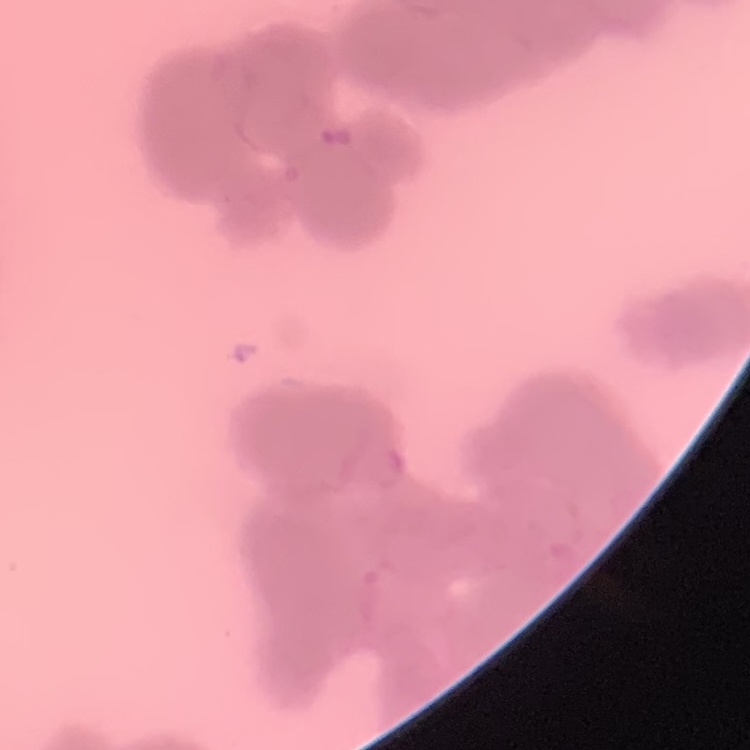

The erythrocytes show rouleaux formation. Square crop of a larger photomicrograph. Thin peripheral smear. Stained with either Field's or Giemsa.